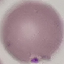

Summary:
  - Result: no malaria parasites detected
  - Preparation: thin blood smear
  - Image type: automatically extracted cell patch, resized to 64 × 64 pixels
  - Stain: Giemsa
  - Capture: smartphone camera at the microscope eyepiece